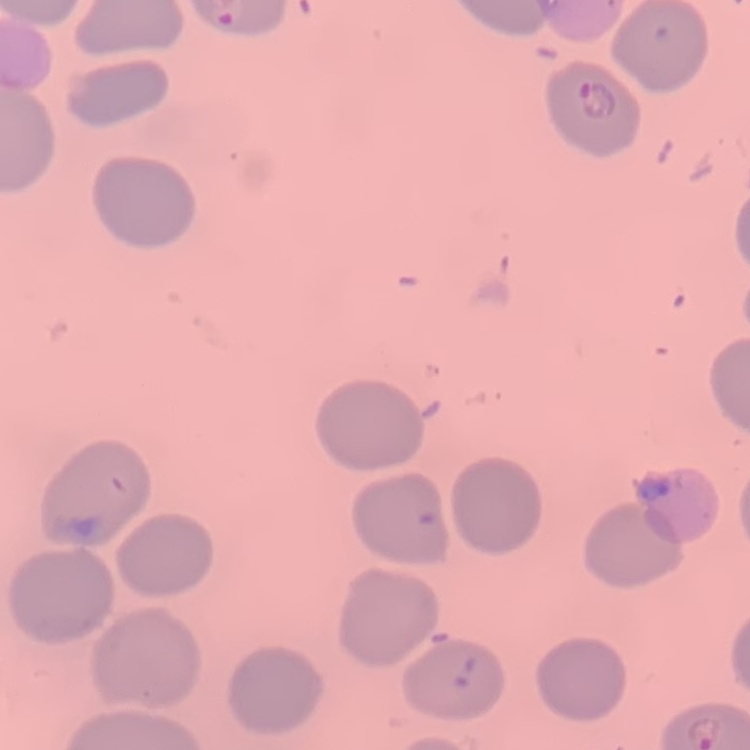

erythrocyte morphology = no rouleaux formation
preparation = thin blood smear
image type = square crop of a larger photomicrograph
stain = Field's or Giemsa